Report the malaria status of this cell.
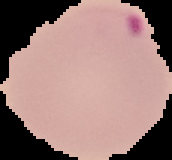

Parasitized.

Segmented cell region on a black background. From a thin blood film. Image is 172×160 pixels.